Locate and identify every blood parasite.
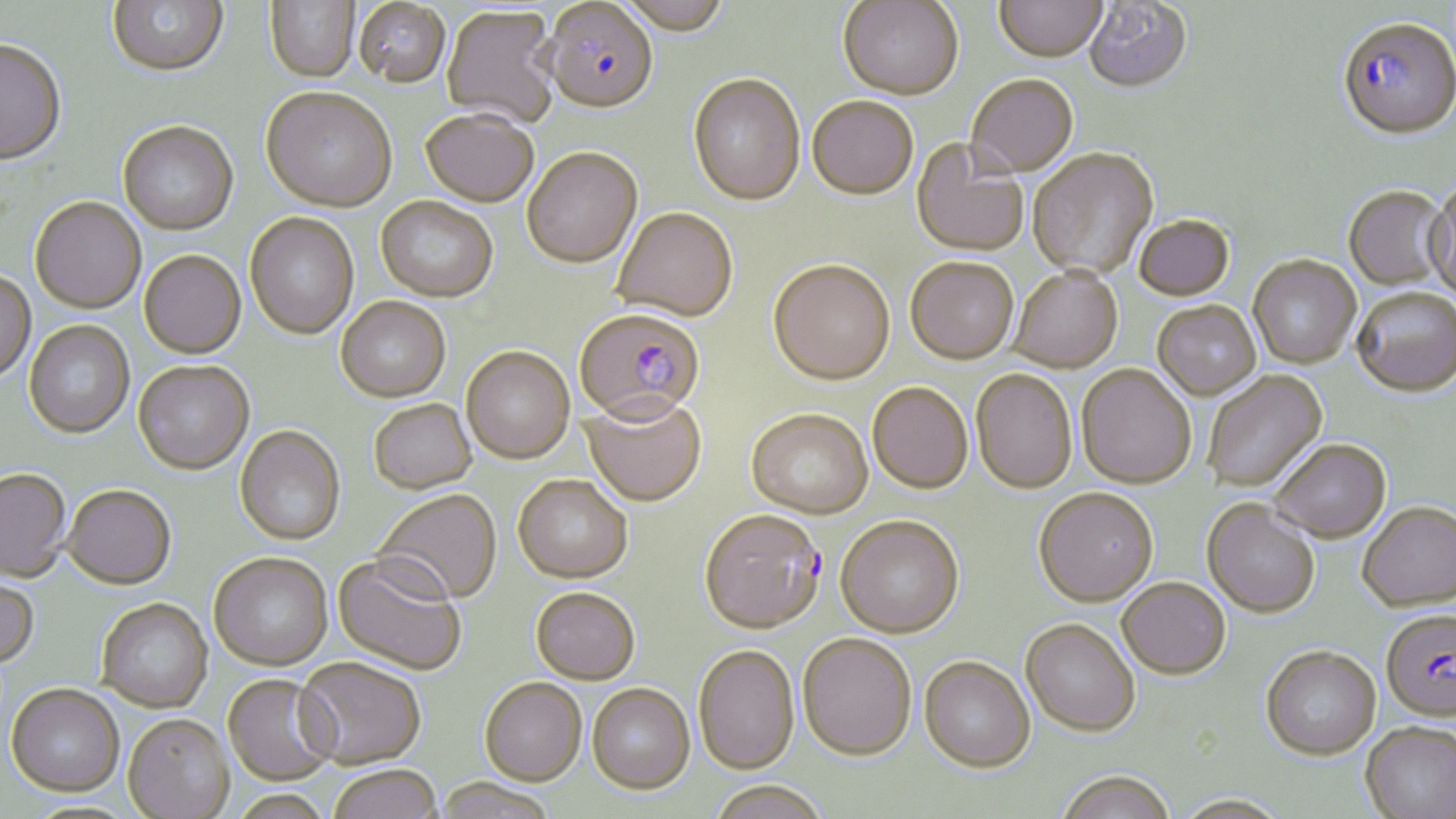

Approximate bounding boxes as [x1, y1, x2, y2] in pixels.
Plasmodium falciparum-infected red blood cells: [543, 3, 658, 117], [1337, 21, 1456, 144], [574, 311, 705, 430], [699, 510, 825, 637], [1381, 612, 1456, 725].
No Plasmodium ovale, Plasmodium malariae, Plasmodium vivax, Babesia divergens, or Trypanosoma brucei observed.

{
  "slide_level_diagnosis": "Plasmodium falciparum",
  "magnification": "1000x",
  "field_of_view": "one of a larger specimen",
  "uninfected_red_blood_cell_locations": "approximate bounding boxes as [x1, y1, x2, y2] in pixels: [107, 0, 229, 80], [615, 0, 734, 37], [994, 0, 1108, 66], [264, 1, 360, 84], [838, 1, 964, 104], [1083, 1, 1193, 97], [353, 2, 452, 92], [442, 8, 561, 129], [0, 42, 66, 168], [688, 76, 806, 210], [966, 77, 1078, 180], [260, 91, 396, 215], [807, 99, 918, 202], [420, 112, 538, 210], [117, 124, 239, 238], [911, 140, 1029, 259], [522, 150, 643, 271], [1029, 150, 1159, 281], [1425, 186, 1456, 305], [1343, 188, 1450, 291], [375, 198, 498, 304], [30, 199, 146, 316], [612, 210, 738, 326], [245, 214, 359, 342], [1134, 217, 1234, 304], [139, 252, 246, 361], [1248, 258, 1361, 370], [905, 260, 1018, 367], [768, 262, 896, 388], [1009, 270, 1123, 375], [0, 272, 36, 388], [1352, 290, 1456, 401], [336, 299, 451, 404], [1152, 303, 1261, 401], [25, 321, 135, 440], [461, 348, 575, 466], [133, 363, 254, 477], [1076, 366, 1196, 491], [971, 371, 1077, 495], [1204, 371, 1328, 494], [867, 384, 972, 495], [581, 397, 706, 509], [369, 401, 477, 496], [745, 411, 873, 521], [234, 428, 346, 547], [1269, 442, 1391, 545], [0, 470, 72, 584], [513, 477, 632, 585], [63, 487, 176, 592], [373, 490, 502, 606], [1034, 490, 1158, 608], [1202, 501, 1320, 620], [1358, 505, 1456, 616], [835, 517, 964, 640], [209, 555, 333, 673], [331, 555, 467, 678], [0, 576, 39, 671], [1117, 580, 1231, 682], [531, 590, 640, 686], [96, 600, 213, 714], [1020, 621, 1140, 740], [798, 635, 916, 762], [693, 646, 800, 775], [1260, 648, 1381, 763], [919, 658, 1036, 775], [294, 660, 426, 771], [222, 675, 338, 787], [479, 679, 587, 787], [587, 684, 696, 795], [5, 687, 124, 800], [123, 717, 235, 819], [1360, 724, 1456, 819], [328, 767, 442, 819], [1055, 775, 1177, 819], [434, 779, 557, 819], [707, 782, 830, 819], [227, 792, 336, 819], [1170, 796, 1292, 819]",
  "image_size": "1456×819 pixels",
  "stain": "May-Grünwald-Giemsa",
  "preparation": "thin blood smear",
  "modality": "light microscopy"
}